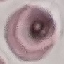

Result: no malaria parasites detected. Thin blood smear. Automatically extracted cell patch, resized to 64 × 64 pixels. Acquired by smartphone through the microscope eyepiece. Giemsa-stained preparation.